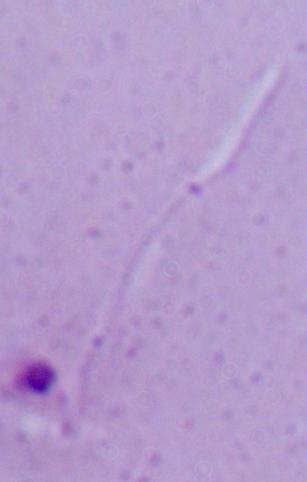

Summary:
  - Identification: Leishmania
  - Modality: micrograph
  - Magnification: 1000x